Outline each blood parasite and name the species.
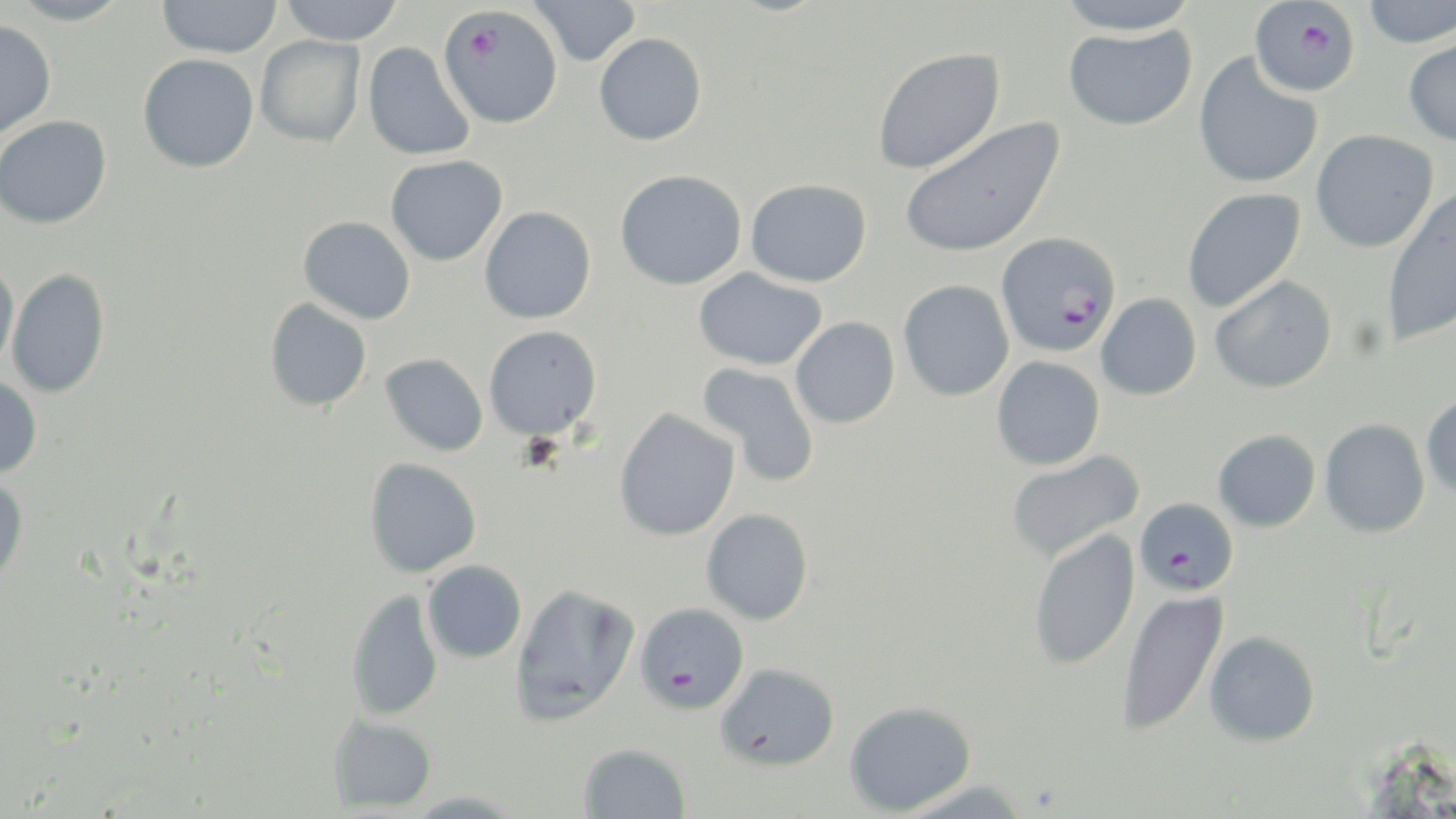
Approximate bounding boxes as (x1, y1, x2, y2) in pixels.
Plasmodium falciparum-infected red blood cells (subset): (1249, 2, 1360, 97), (438, 5, 564, 128), (996, 231, 1121, 357), (1133, 498, 1239, 596).
No Plasmodium ovale, Plasmodium malariae, Plasmodium vivax, Babesia divergens, or Trypanosoma brucei observed.

Summary:
  - Uninfected red blood cell locations (subset): (9, 0, 130, 26), (158, 0, 282, 58), (279, 0, 404, 45), (529, 0, 641, 67), (1055, 0, 1199, 35), (1360, 0, 1456, 48), (0, 20, 56, 138), (1063, 25, 1196, 130), (594, 33, 707, 145), (1402, 34, 1456, 147), (255, 35, 365, 147), (363, 42, 475, 160), (872, 47, 1004, 174), (138, 53, 259, 172), (1193, 53, 1323, 189), (0, 115, 112, 229), (898, 117, 1065, 258), (1310, 130, 1438, 253), (386, 154, 507, 266), (615, 169, 746, 289), (746, 179, 871, 287), (1181, 187, 1306, 313), (1380, 189, 1456, 347), (479, 206, 596, 324), (298, 216, 415, 324), (0, 259, 19, 372), (693, 267, 826, 370), (6, 268, 109, 397), (1209, 275, 1337, 393), (898, 279, 1014, 401), (1096, 293, 1202, 400), (264, 298, 372, 412), (791, 317, 900, 428), (483, 325, 602, 440), (380, 353, 489, 456), (991, 356, 1105, 470), (697, 361, 821, 487), (0, 376, 43, 478), (1420, 391, 1456, 499), (614, 408, 740, 541), (1319, 419, 1430, 537), (1212, 430, 1321, 532), (1006, 451, 1144, 562), (364, 457, 482, 577), (0, 475, 28, 588), (701, 508, 814, 625), (1028, 528, 1140, 670), (422, 560, 527, 663), (510, 582, 640, 726), (1117, 588, 1229, 737), (347, 589, 443, 721), (1204, 630, 1320, 746), (716, 663, 839, 770), (844, 701, 976, 816), (328, 715, 437, 813), (578, 742, 691, 818), (894, 779, 1034, 818)
  - Slide-level diagnosis: Plasmodium falciparum
  - Modality: optical microscopy
  - Image size: 1456×819 pixels
  - Preparation: thin blood film
  - Stain: May-Grünwald-Giemsa
  - Magnification: 1000x
  - Field of view: single